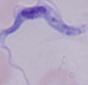

A trypanosome is seen. 1000x magnification. Micrograph.